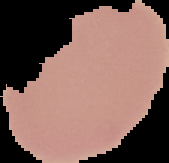
Result: negative for Plasmodium parasites. Segmented cell region on a black background. Image is 169×163 pixels. From a thin blood smear.